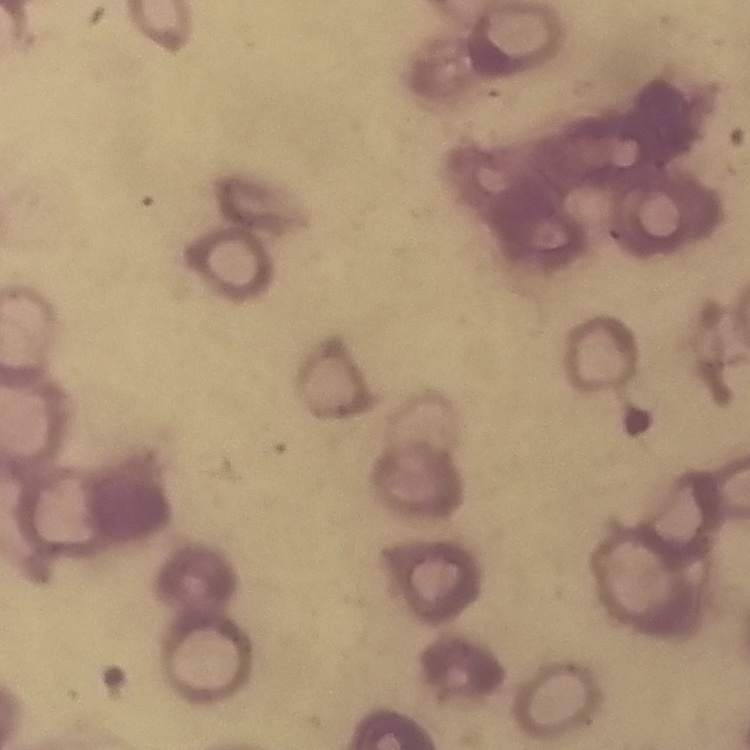
Summary:
  - Erythrocyte morphology: rouleaux formation
  - Image type: square crop of a larger photomicrograph
  - Stain: Field's or Giemsa
  - Preparation: thin blood film